Classify this cell by malaria status.
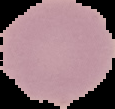

Uninfected.

Summary:
  - Image size: 115×109 pixels
  - Preparation: thin blood smear
  - Image type: segmented cell region with the area outside set to black